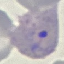
malaria_status: parasitized
preparation: thin smear
capture: smartphone camera at the microscope eyepiece
image_type: automatically extracted cell patch, resized to 64 × 64 pixels
stain: Giemsa